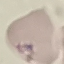 Result: no malaria parasites detected. Thin blood smear. Giemsa stain. Acquired by smartphone through the microscope eyepiece. Cell patch, automatically extracted from a larger field of view and resized to 64 × 64 pixels.